Identify the parasite.
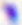

Toxoplasma gondii.

magnification = 400x
modality = photomicrograph